Name the parasite shown.
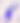

Toxoplasma gondii.

Captured at 400x magnification. Micrograph.